Identify the parasite.
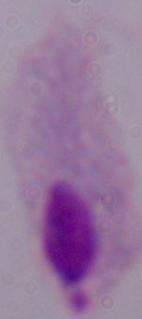
A trichomonad.

Captured at 1000x magnification. Photomicrograph.